Locate every Plasmodium parasite.
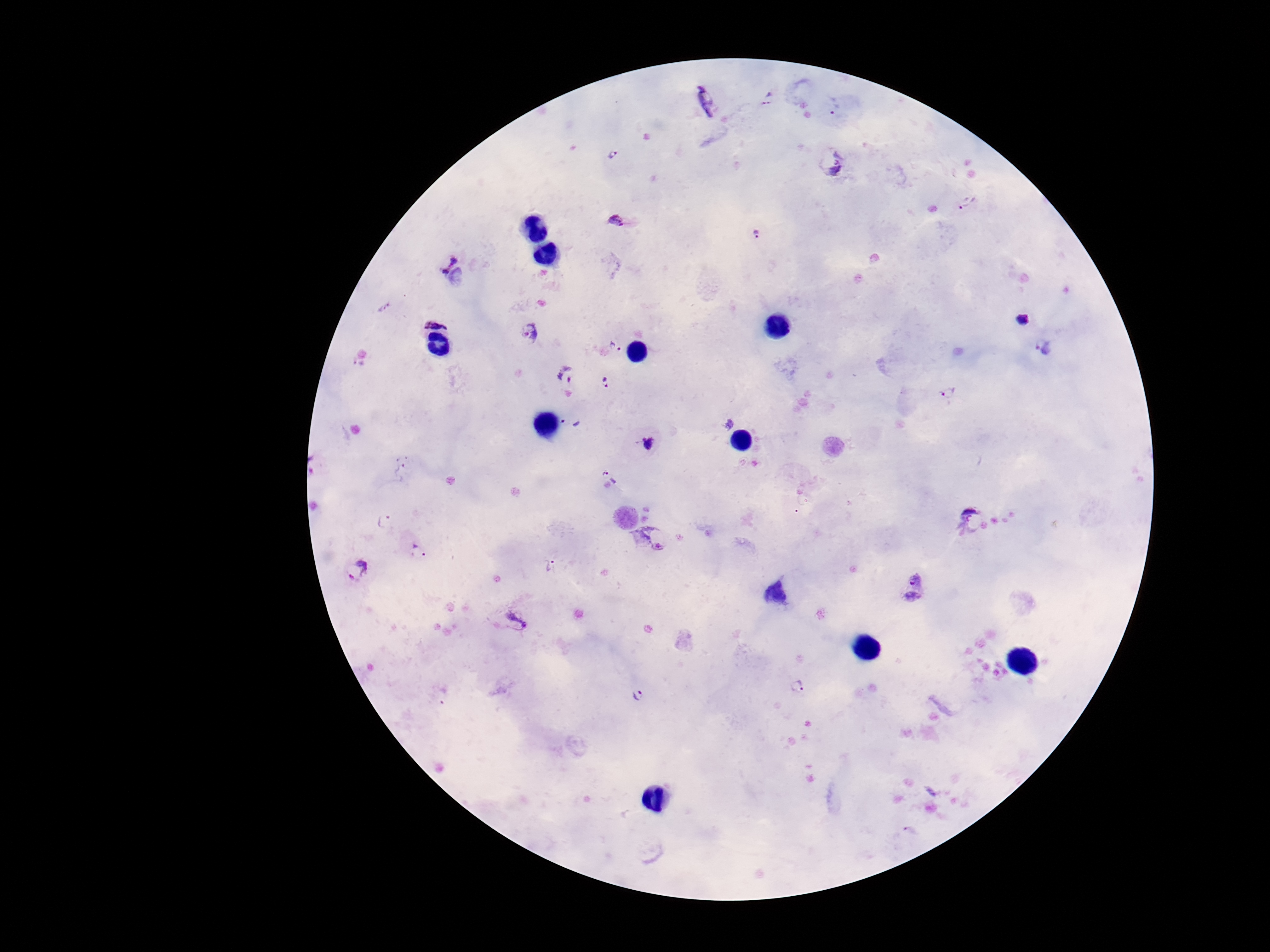
Approximate object centers, in pixels from the top-left corner.
Plasmodium parasites: (x=768, y=99), (x=707, y=103), (x=835, y=107), (x=612, y=155), (x=832, y=160), (x=969, y=202), (x=616, y=223), (x=758, y=235), (x=446, y=261), (x=437, y=313), (x=1022, y=319), (x=532, y=332), (x=1045, y=345), (x=615, y=347), (x=565, y=372), (x=607, y=384), (x=948, y=392), (x=570, y=422), (x=648, y=444), (x=403, y=471), (x=604, y=471), (x=974, y=520), (x=384, y=521), (x=650, y=540), (x=418, y=552), (x=552, y=567), (x=357, y=571), (x=913, y=589), (x=517, y=622), (x=798, y=688), (x=638, y=694).

Summary:
  - Magnification: 100x
  - Preparation: thick blood smear
  - Field of view: single
  - Stain: Giemsa
  - Image size: 1270×952 pixels
  - Capture: smartphone camera through the microscope eyepiece
  - Patient malaria status: infected